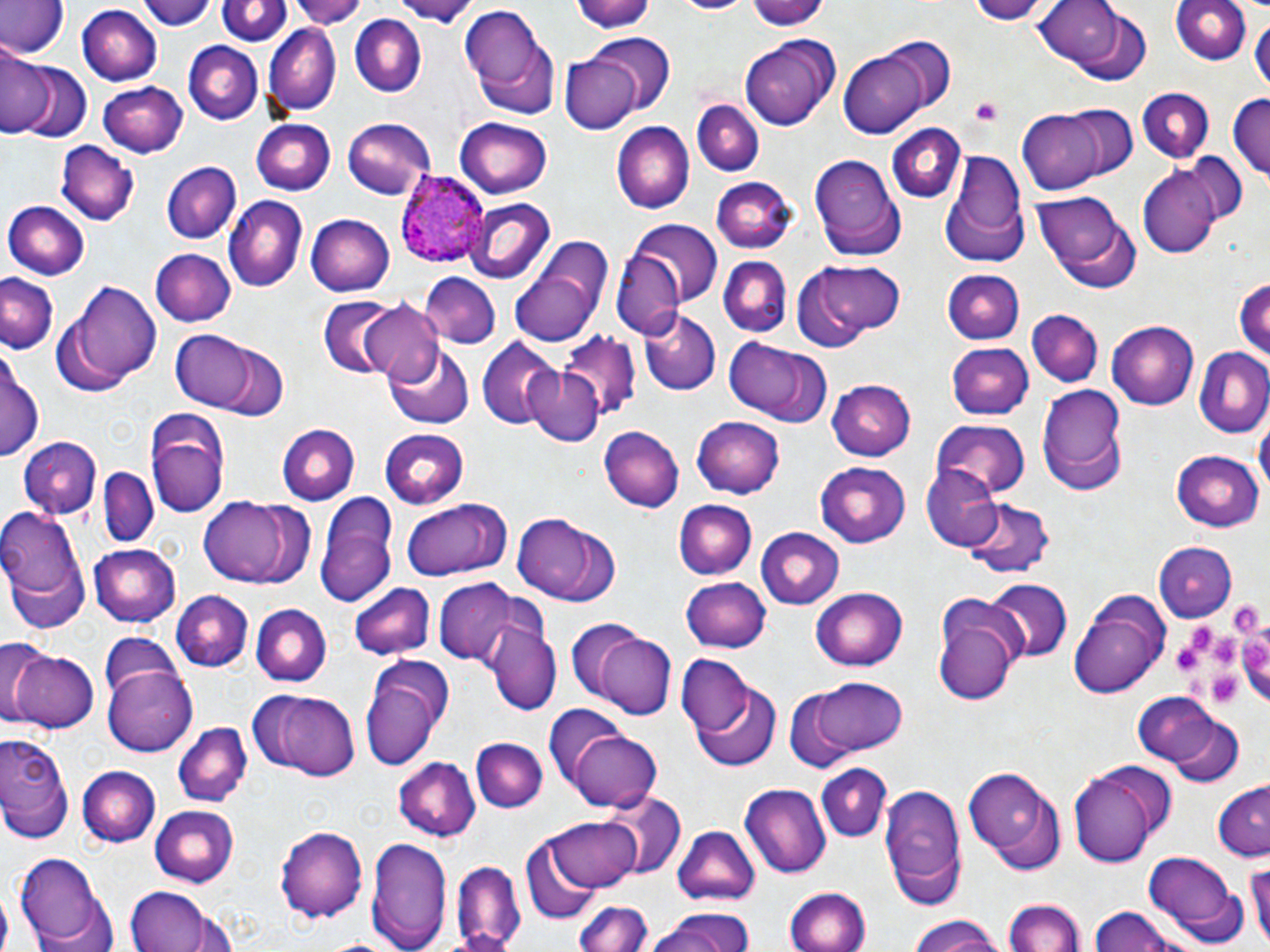
Summary:
  - Coordinate format: approximate bounding boxes as named x1/y1/x2/y2 corners in pixels
  - Plasmodium ovale-infected red blood cell locations: (x1=393, y1=167, x2=492, y2=269)
  - Platelet locations: (x1=970, y1=98, x2=1005, y2=127), (x1=1227, y1=600, x2=1264, y2=638), (x1=1172, y1=631, x2=1209, y2=678), (x1=1206, y1=634, x2=1242, y2=669), (x1=1242, y1=635, x2=1270, y2=676), (x1=1207, y1=675, x2=1244, y2=705)
  - Uninfected red blood cell locations: (x1=143, y1=0, x2=218, y2=31), (x1=218, y1=0, x2=288, y2=47), (x1=288, y1=0, x2=368, y2=26), (x1=397, y1=0, x2=478, y2=29), (x1=576, y1=0, x2=658, y2=34), (x1=672, y1=0, x2=750, y2=16), (x1=968, y1=0, x2=1051, y2=25), (x1=1034, y1=0, x2=1133, y2=74), (x1=1172, y1=0, x2=1253, y2=67), (x1=0, y1=1, x2=65, y2=59), (x1=748, y1=1, x2=830, y2=32), (x1=457, y1=3, x2=557, y2=113), (x1=76, y1=5, x2=161, y2=84), (x1=349, y1=14, x2=426, y2=97), (x1=1251, y1=14, x2=1268, y2=98), (x1=263, y1=26, x2=340, y2=115), (x1=587, y1=35, x2=675, y2=116), (x1=738, y1=35, x2=839, y2=132), (x1=871, y1=37, x2=957, y2=125), (x1=184, y1=41, x2=263, y2=125), (x1=0, y1=50, x2=49, y2=138), (x1=838, y1=50, x2=931, y2=138), (x1=561, y1=55, x2=641, y2=136), (x1=14, y1=62, x2=92, y2=144), (x1=99, y1=79, x2=190, y2=156), (x1=1135, y1=85, x2=1216, y2=163), (x1=1229, y1=93, x2=1270, y2=185), (x1=692, y1=100, x2=762, y2=176), (x1=1061, y1=104, x2=1140, y2=182), (x1=1017, y1=111, x2=1107, y2=194), (x1=452, y1=115, x2=553, y2=196), (x1=342, y1=116, x2=437, y2=199), (x1=251, y1=117, x2=337, y2=194), (x1=614, y1=121, x2=695, y2=212), (x1=885, y1=124, x2=968, y2=204), (x1=60, y1=142, x2=137, y2=226), (x1=942, y1=149, x2=1029, y2=263), (x1=807, y1=152, x2=906, y2=262), (x1=1186, y1=154, x2=1247, y2=226), (x1=161, y1=162, x2=240, y2=245), (x1=1138, y1=164, x2=1222, y2=259), (x1=713, y1=176, x2=796, y2=252), (x1=1032, y1=191, x2=1138, y2=291), (x1=222, y1=197, x2=306, y2=293), (x1=461, y1=197, x2=555, y2=283), (x1=4, y1=202, x2=90, y2=280), (x1=304, y1=211, x2=396, y2=298), (x1=630, y1=220, x2=722, y2=305), (x1=510, y1=241, x2=613, y2=347), (x1=152, y1=248, x2=235, y2=326), (x1=614, y1=252, x2=682, y2=340), (x1=718, y1=256, x2=792, y2=338), (x1=803, y1=260, x2=907, y2=340), (x1=943, y1=269, x2=1026, y2=344), (x1=419, y1=274, x2=500, y2=348), (x1=0, y1=275, x2=56, y2=355), (x1=1234, y1=275, x2=1269, y2=367), (x1=71, y1=281, x2=164, y2=385), (x1=318, y1=297, x2=404, y2=379), (x1=360, y1=302, x2=445, y2=385), (x1=641, y1=306, x2=721, y2=396), (x1=1026, y1=310, x2=1104, y2=388), (x1=1105, y1=319, x2=1197, y2=409), (x1=171, y1=330, x2=257, y2=411), (x1=556, y1=334, x2=641, y2=423), (x1=723, y1=335, x2=829, y2=425), (x1=479, y1=338, x2=560, y2=430), (x1=205, y1=340, x2=291, y2=422), (x1=946, y1=341, x2=1034, y2=419), (x1=385, y1=343, x2=473, y2=428), (x1=1194, y1=346, x2=1270, y2=439), (x1=0, y1=350, x2=43, y2=466), (x1=522, y1=363, x2=606, y2=448), (x1=826, y1=379, x2=914, y2=462), (x1=1036, y1=383, x2=1127, y2=494), (x1=144, y1=408, x2=228, y2=519), (x1=1255, y1=413, x2=1269, y2=504), (x1=691, y1=416, x2=785, y2=499), (x1=930, y1=419, x2=1030, y2=496), (x1=277, y1=424, x2=358, y2=505), (x1=598, y1=424, x2=684, y2=513), (x1=378, y1=428, x2=469, y2=507), (x1=17, y1=438, x2=100, y2=517), (x1=1171, y1=450, x2=1263, y2=532), (x1=814, y1=459, x2=912, y2=546), (x1=922, y1=465, x2=1002, y2=549), (x1=97, y1=467, x2=158, y2=545), (x1=316, y1=493, x2=400, y2=609), (x1=200, y1=497, x2=310, y2=589), (x1=962, y1=498, x2=1053, y2=579), (x1=401, y1=499, x2=511, y2=582), (x1=675, y1=501, x2=757, y2=580), (x1=0, y1=505, x2=87, y2=612), (x1=510, y1=512, x2=619, y2=606), (x1=756, y1=528, x2=844, y2=609), (x1=1153, y1=541, x2=1236, y2=622), (x1=88, y1=543, x2=181, y2=626), (x1=680, y1=575, x2=770, y2=652), (x1=983, y1=579, x2=1071, y2=665), (x1=434, y1=580, x2=520, y2=667), (x1=349, y1=582, x2=434, y2=661), (x1=812, y1=586, x2=907, y2=671), (x1=1069, y1=590, x2=1169, y2=699), (x1=170, y1=591, x2=254, y2=671), (x1=932, y1=593, x2=1023, y2=702), (x1=249, y1=604, x2=332, y2=687), (x1=486, y1=619, x2=559, y2=716), (x1=565, y1=621, x2=652, y2=705), (x1=592, y1=629, x2=676, y2=718), (x1=99, y1=633, x2=179, y2=712), (x1=0, y1=643, x2=59, y2=725), (x1=8, y1=649, x2=99, y2=735), (x1=680, y1=650, x2=765, y2=746), (x1=360, y1=654, x2=456, y2=770), (x1=103, y1=663, x2=197, y2=756), (x1=689, y1=677, x2=781, y2=775), (x1=811, y1=677, x2=908, y2=756), (x1=262, y1=689, x2=361, y2=781), (x1=784, y1=689, x2=857, y2=772), (x1=1133, y1=690, x2=1229, y2=772), (x1=543, y1=706, x2=624, y2=793), (x1=1162, y1=714, x2=1245, y2=787), (x1=173, y1=722, x2=252, y2=806), (x1=567, y1=727, x2=661, y2=811), (x1=0, y1=729, x2=74, y2=841), (x1=472, y1=737, x2=547, y2=812), (x1=393, y1=757, x2=480, y2=842), (x1=1066, y1=761, x2=1173, y2=867), (x1=815, y1=764, x2=890, y2=842), (x1=76, y1=765, x2=160, y2=846), (x1=962, y1=765, x2=1066, y2=872), (x1=880, y1=782, x2=965, y2=904), (x1=1214, y1=782, x2=1269, y2=859), (x1=740, y1=784, x2=830, y2=881), (x1=599, y1=792, x2=686, y2=880), (x1=150, y1=804, x2=241, y2=883), (x1=547, y1=813, x2=640, y2=893), (x1=275, y1=825, x2=369, y2=924), (x1=674, y1=825, x2=761, y2=908), (x1=367, y1=835, x2=451, y2=952), (x1=519, y1=841, x2=604, y2=924), (x1=15, y1=850, x2=108, y2=946), (x1=1245, y1=853, x2=1270, y2=950), (x1=1143, y1=854, x2=1248, y2=945), (x1=451, y1=859, x2=525, y2=951), (x1=123, y1=884, x2=233, y2=952), (x1=785, y1=887, x2=871, y2=952), (x1=1005, y1=897, x2=1084, y2=951), (x1=578, y1=901, x2=653, y2=952), (x1=1087, y1=908, x2=1187, y2=952), (x1=643, y1=909, x2=760, y2=952), (x1=905, y1=913, x2=1008, y2=952)
  - Slide-level diagnosis: Plasmodium ovale
  - Stain: May-Grünwald-Giemsa
  - Image size: 1270×952 pixels
  - Modality: light microscopy
  - Field of view: one of a larger specimen
  - Magnification: 1000x
  - Preparation: thin blood film